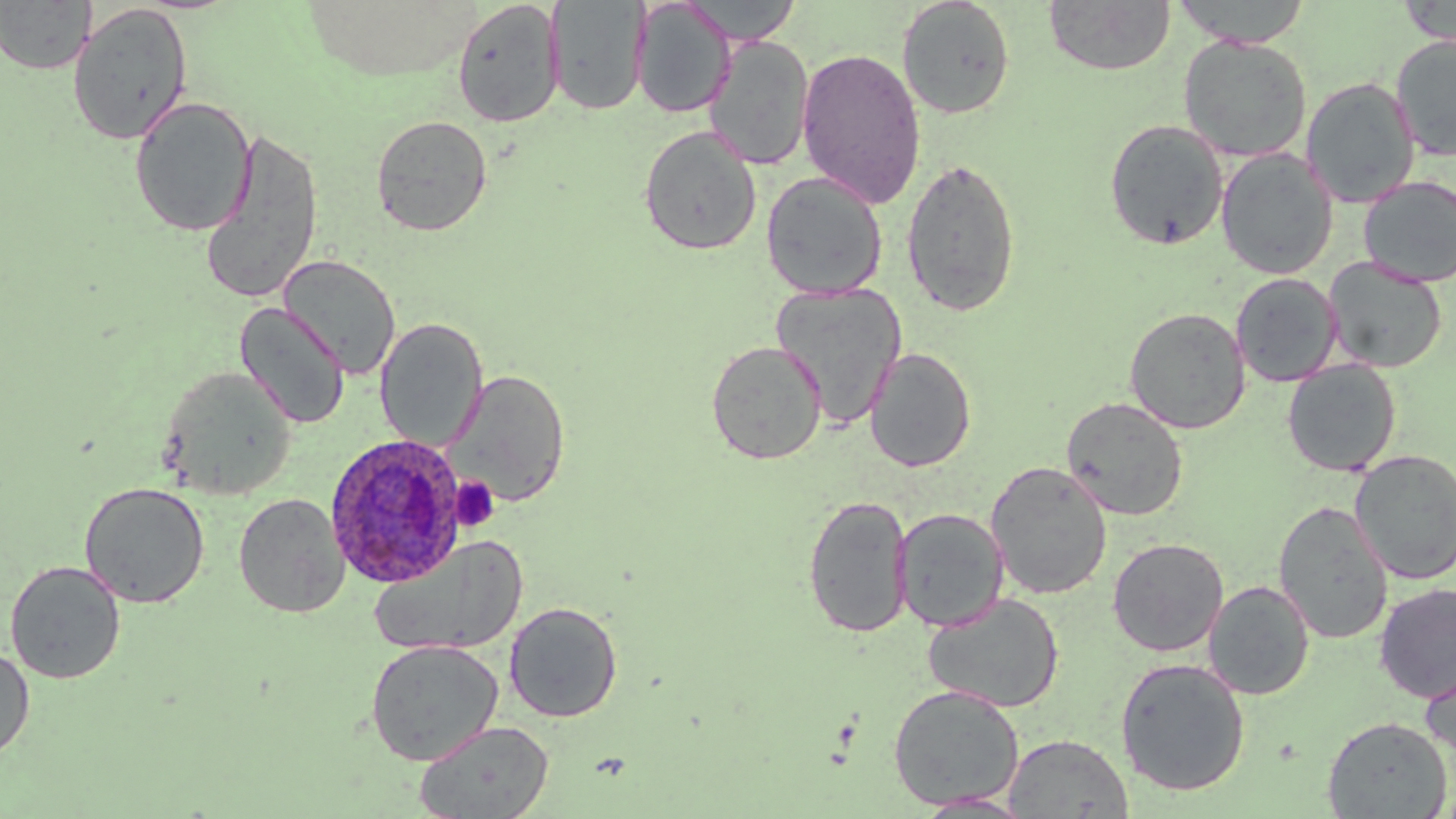
{
  "slide_level_diagnosis": "Plasmodium ovale",
  "platelet_locations": "approximate bounding boxes as (x1, y1, x2, y2) in pixels: (450, 476, 500, 531)",
  "image_size": "1456×819 pixels",
  "preparation": "thin blood smear",
  "plasmodium_ovale_infected_red_blood_cell_locations": "approximate bounding boxes as (x1, y1, x2, y2) in pixels: (325, 433, 467, 588)",
  "stain": "May-Grünwald-Giemsa",
  "magnification": "1000x",
  "uninfected_red_blood_cell_locations": "approximate bounding boxes as (x1, y1, x2, y2) in pixels: (0, 0, 95, 75), (680, 0, 803, 42), (897, 0, 1016, 120), (1171, 0, 1313, 48), (452, 1, 564, 128), (548, 1, 649, 116), (632, 1, 734, 118), (1043, 1, 1176, 75), (1399, 1, 1455, 46), (67, 2, 194, 146), (1390, 33, 1456, 160), (705, 35, 814, 170), (1178, 36, 1312, 162), (796, 47, 925, 208), (1301, 76, 1421, 208), (130, 96, 256, 237), (371, 114, 494, 236), (1103, 118, 1230, 250), (638, 125, 762, 256), (198, 127, 324, 305), (1216, 149, 1338, 280), (900, 157, 1022, 317), (761, 171, 888, 299), (1357, 175, 1456, 287), (278, 255, 401, 379), (1322, 257, 1447, 373), (1231, 273, 1342, 387), (770, 283, 908, 429), (234, 303, 350, 429), (1124, 307, 1250, 434), (374, 317, 488, 451), (705, 340, 827, 465), (864, 348, 977, 472), (1282, 360, 1401, 476), (159, 366, 297, 500), (448, 369, 571, 507), (1061, 396, 1189, 521), (1349, 449, 1456, 585), (985, 461, 1112, 600), (79, 481, 210, 608), (234, 493, 350, 618), (803, 494, 913, 638), (1273, 500, 1394, 644), (894, 508, 1009, 632), (369, 536, 529, 658), (1107, 537, 1229, 657), (4, 560, 126, 685), (1204, 580, 1314, 700), (1374, 582, 1456, 703), (922, 592, 1064, 713), (504, 601, 623, 723), (365, 639, 504, 766), (0, 645, 35, 761), (1420, 654, 1456, 771), (1114, 656, 1251, 796), (887, 683, 1025, 810), (1322, 715, 1451, 818), (413, 719, 555, 819), (1003, 733, 1133, 818), (913, 791, 1036, 817)",
  "field_of_view": "single",
  "modality": "optical microscopy"
}